State which parasite is depicted.
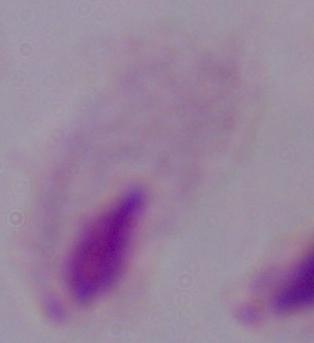

A trichomonad.

Captured at 1000x magnification. Micrograph.